Describe the morphology of the erythrocytes.
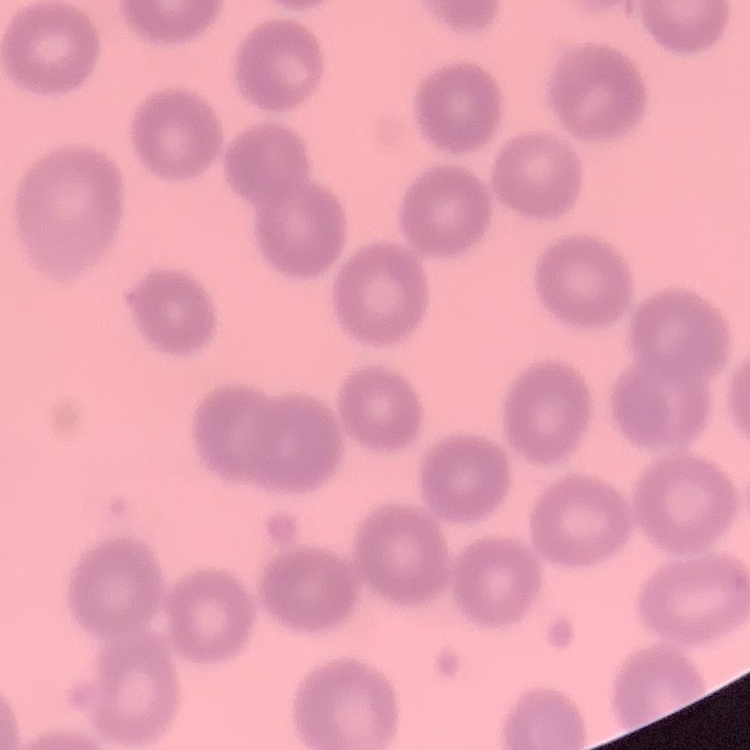

They show no rouleaux formation.

preparation = thin peripheral smear
stain = Field's or Giemsa
image type = square crop of a larger photomicrograph